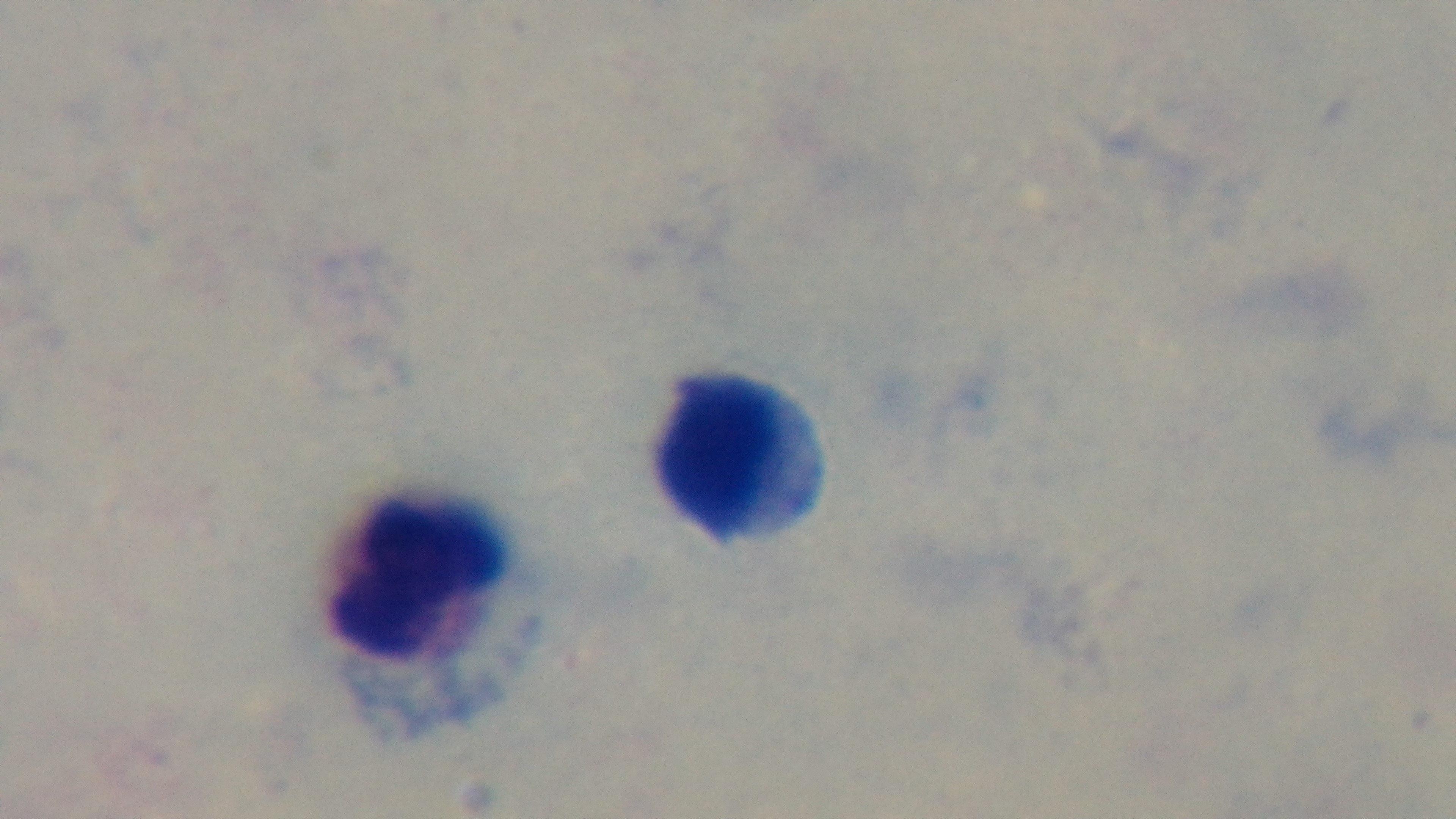
Oil-immersion objective, 100x. Preparation: thick smear. Malaria status: uninfected. Light microscopy. Captured with a mounted 4K digital camera. Single field of view. Giemsa stain.